Comment on the morphology of the red blood cells.
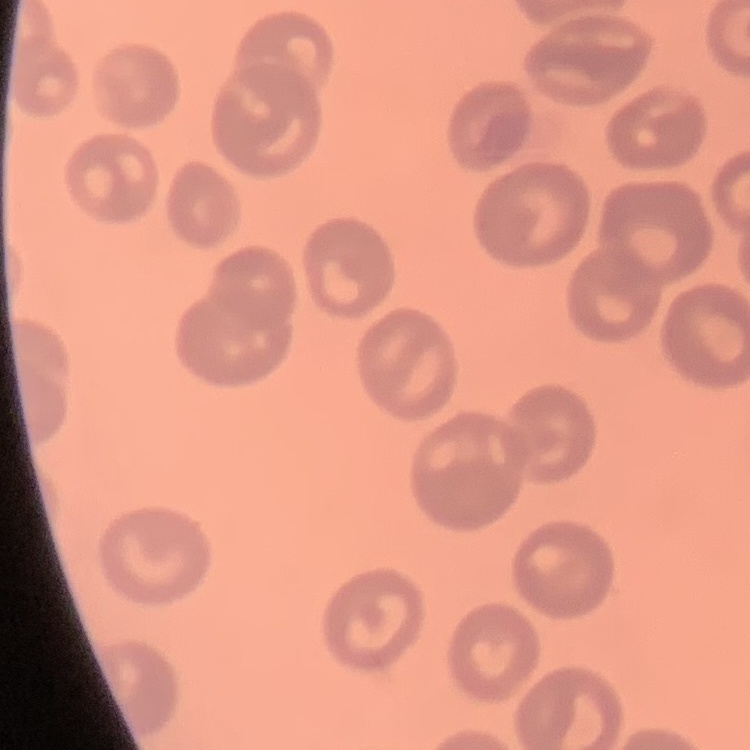

No rouleaux formation.

preparation = thin blood smear
stain = Field's or Giemsa
image type = square crop of a larger photomicrograph